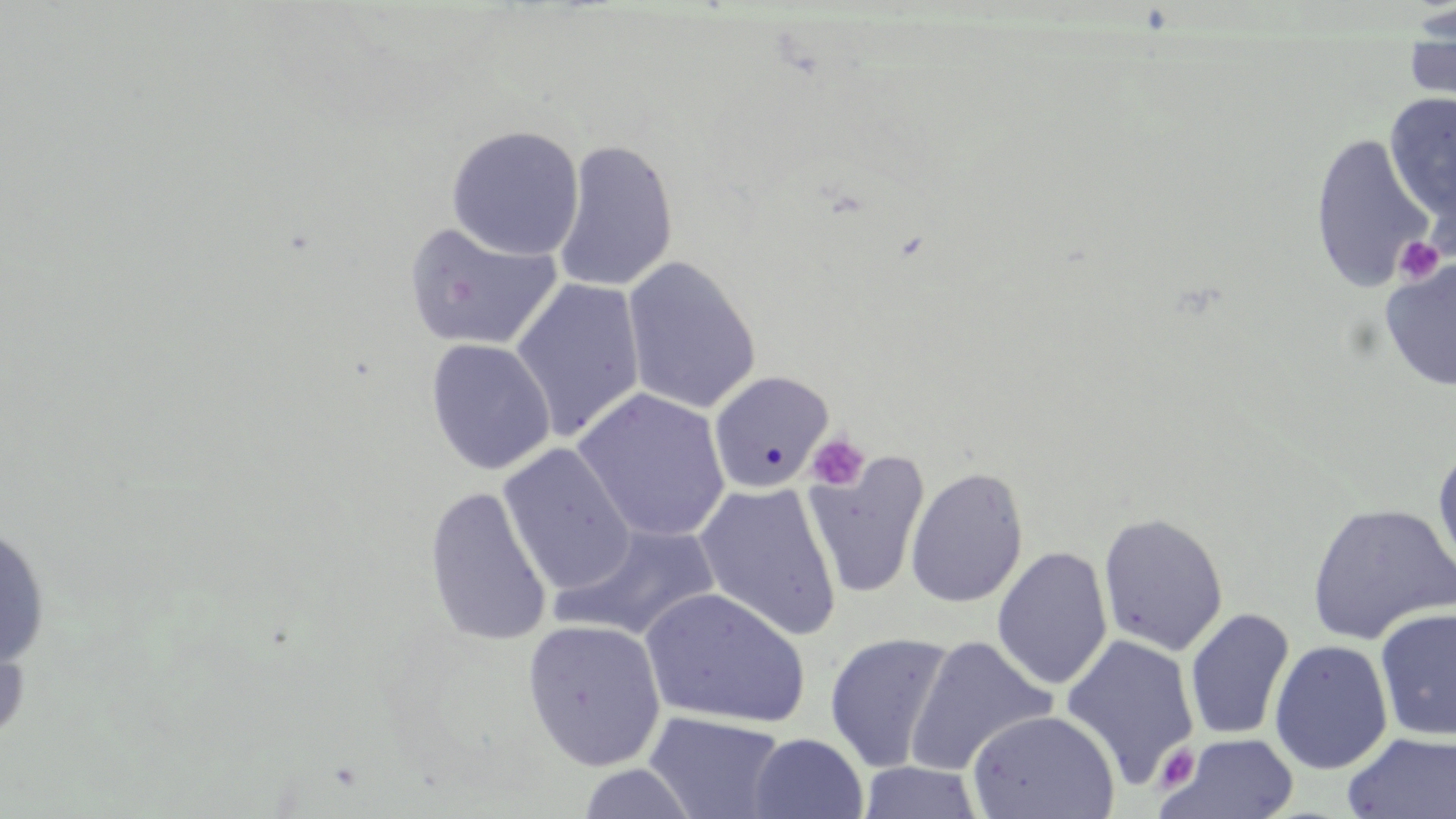
Approximate bounding boxes as named x1/y1/x2/y2 corners in pixels. Uninfected red blood cell locations: (x1=1401, y1=9, x2=1456, y2=120), (x1=1384, y1=91, x2=1456, y2=228), (x1=445, y1=124, x2=585, y2=261), (x1=1309, y1=132, x2=1434, y2=295), (x1=552, y1=139, x2=678, y2=292), (x1=403, y1=221, x2=562, y2=352), (x1=622, y1=256, x2=761, y2=415), (x1=1379, y1=256, x2=1456, y2=393), (x1=510, y1=277, x2=646, y2=442), (x1=425, y1=338, x2=555, y2=475), (x1=708, y1=370, x2=834, y2=494), (x1=573, y1=388, x2=731, y2=542), (x1=498, y1=443, x2=636, y2=597), (x1=1432, y1=445, x2=1456, y2=581), (x1=805, y1=452, x2=929, y2=600), (x1=905, y1=466, x2=1029, y2=608), (x1=695, y1=482, x2=842, y2=641), (x1=423, y1=485, x2=553, y2=648), (x1=1305, y1=501, x2=1456, y2=645), (x1=1097, y1=512, x2=1229, y2=656), (x1=550, y1=522, x2=722, y2=644), (x1=0, y1=523, x2=51, y2=670), (x1=992, y1=545, x2=1113, y2=690), (x1=639, y1=587, x2=811, y2=730), (x1=1374, y1=606, x2=1456, y2=742), (x1=1184, y1=607, x2=1295, y2=741), (x1=0, y1=611, x2=33, y2=751), (x1=522, y1=619, x2=667, y2=771), (x1=824, y1=632, x2=955, y2=773), (x1=1060, y1=633, x2=1200, y2=790), (x1=905, y1=635, x2=1056, y2=775), (x1=1268, y1=639, x2=1394, y2=776), (x1=968, y1=709, x2=1120, y2=818), (x1=645, y1=712, x2=788, y2=818), (x1=1343, y1=731, x2=1456, y2=819), (x1=749, y1=733, x2=868, y2=819), (x1=1159, y1=733, x2=1300, y2=819), (x1=858, y1=761, x2=983, y2=818). Platelet locations: (x1=1393, y1=236, x2=1446, y2=286), (x1=807, y1=433, x2=870, y2=490), (x1=1158, y1=745, x2=1198, y2=788). Slide-level diagnosis: negative for blood parasites. Image is 1456×819 pixels. Light microscopy. 1000x magnification. May-Grünwald-Giemsa stain. Thin blood smear. Single field of view.